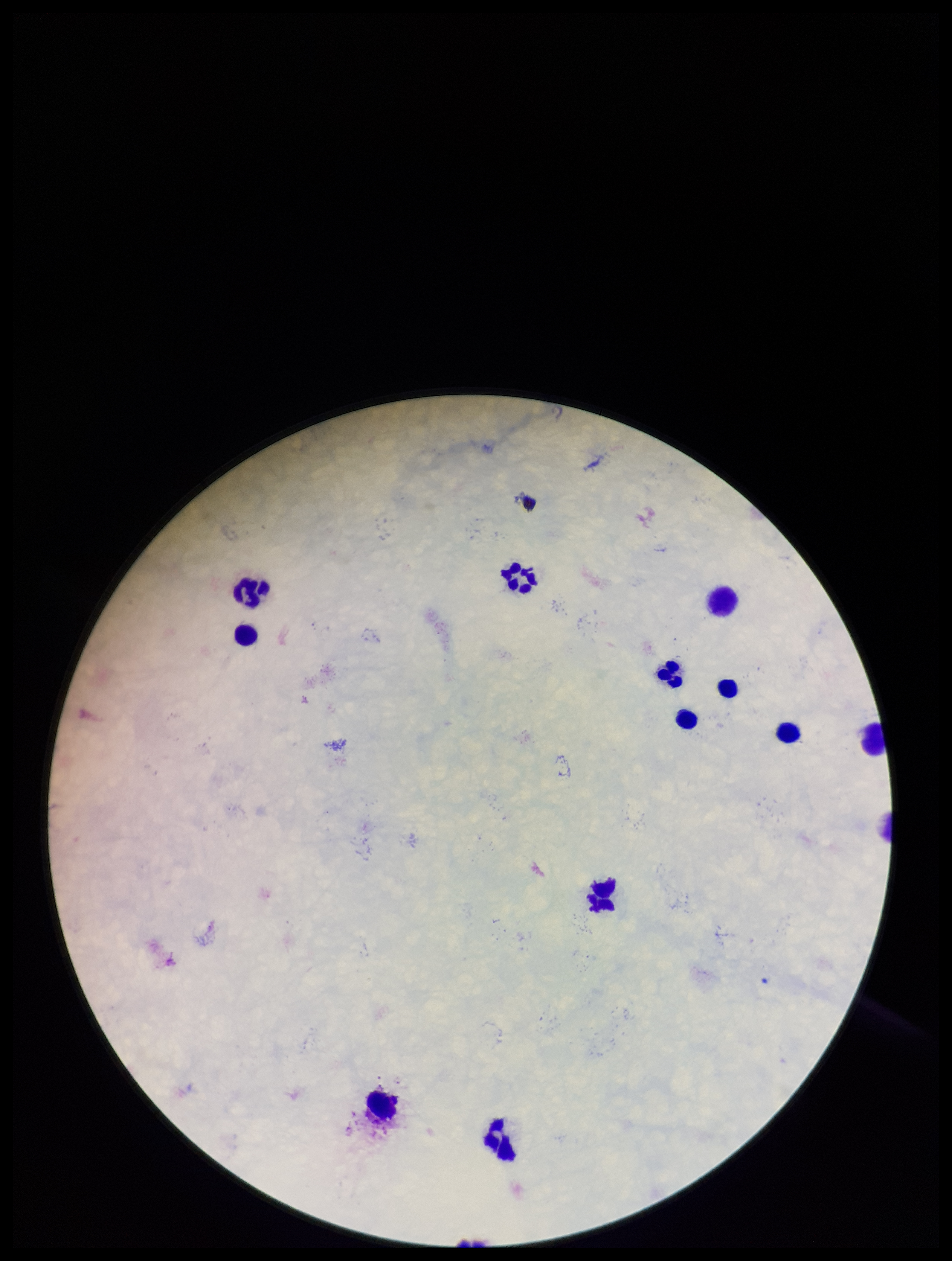
Summary:
  - Image size: 952×1261 pixels
  - Field of view: one from this slide
  - Parasite count: 0
  - Stain: Giemsa
  - Patient malaria status: negative
  - Plasmodium parasites: none identified
  - Leukocyte count: 12
  - Preparation: thick blood smear
  - Capture: smartphone photograph through the microscope eyepiece